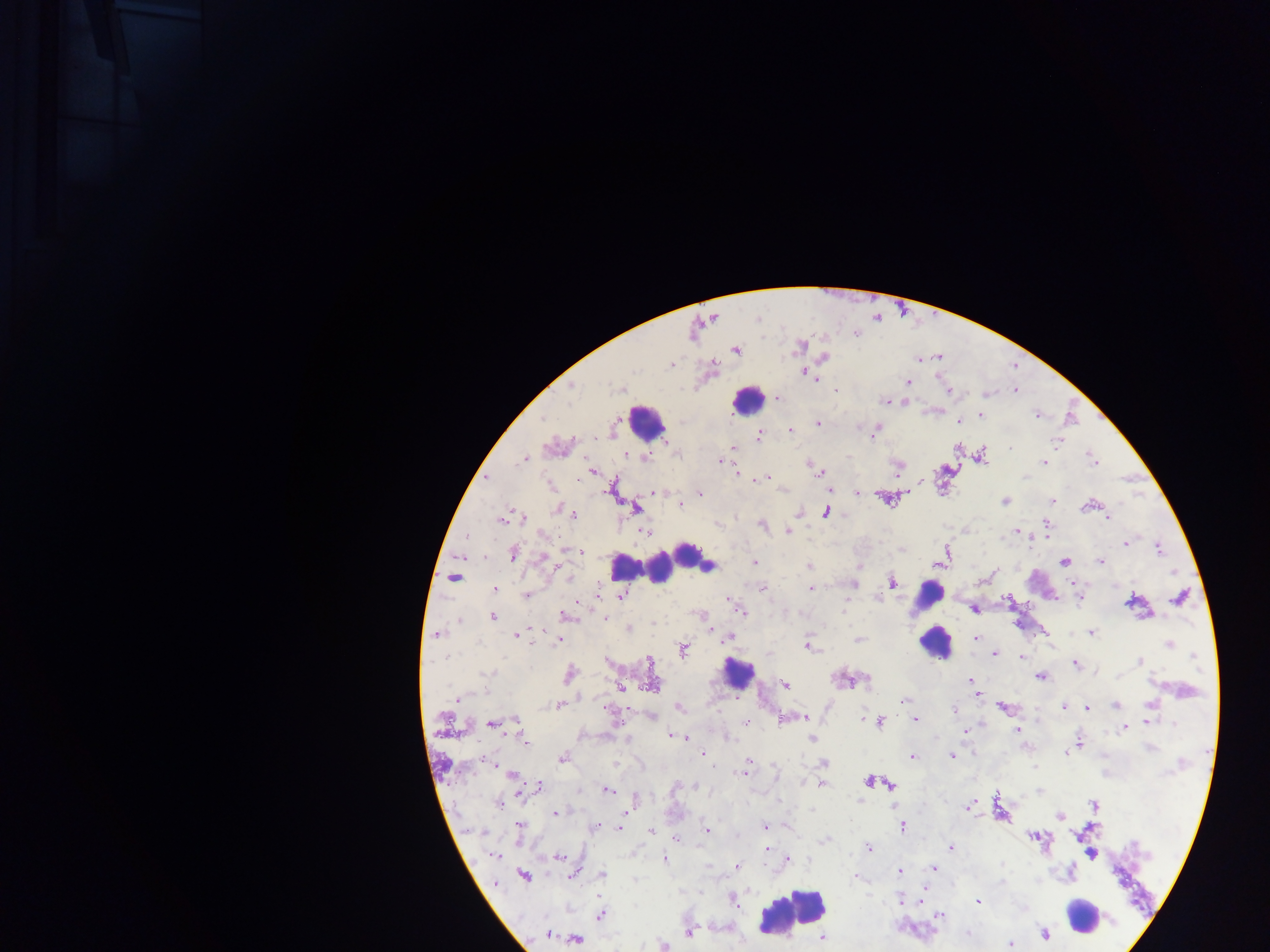

{
  "capture": "mobile-phone photograph through a microscope",
  "plasmodium_parasite_locations": "approximate centers as {x, y} in pixels: {736, 351}, {824, 358}, {671, 364}, {805, 373}, {907, 382}, {570, 387}, {620, 389}, {835, 390}, {1015, 390}, {949, 392}, {778, 398}, {885, 401}, {980, 414}, {1036, 415}, {541, 419}, {958, 421}, {818, 423}, {790, 430}, {874, 431}, {760, 436}, {1058, 442}, {734, 448}, {626, 453}, {981, 456}, {647, 458}, {1093, 458}, {523, 460}, {722, 461}, {1044, 462}, {898, 466}, {592, 471}, {820, 472}, {736, 473}, {1025, 476}, {766, 477}, {486, 478}, {550, 485}, {611, 488}, {657, 492}, {857, 493}, {701, 494}, {885, 498}, {1052, 500}, {1005, 501}, {680, 505}, {1086, 506}, {558, 509}, {635, 509}, {798, 512}, {826, 513}, {573, 515}, {1107, 517}, {523, 518}, {501, 520}, {762, 525}, {1046, 525}, {788, 531}, {1017, 531}, {644, 532}, {544, 535}, {1125, 543}, {1158, 548}, {570, 550}, {579, 551}, {513, 553}, {544, 557}, {1101, 561}, {755, 562}, {1064, 562}, {809, 566}, {454, 577}, {569, 578}, {891, 582}, {853, 585}, {763, 588}, {495, 589}, {811, 589}, {527, 594}, {621, 596}, {1079, 598}, {1179, 598}, {1132, 602}, {844, 609}, {973, 609}, {740, 611}, {567, 615}, {699, 615}, {493, 617}, {605, 619}, {460, 620}, {629, 629}, {1092, 633}, {437, 634}, {516, 635}, {728, 637}, {976, 638}, {858, 639}, {558, 640}, {1170, 644}, {808, 645}, {683, 649}, {995, 653}, {1021, 657}, {649, 661}, {1140, 661}, {1076, 665}, {486, 674}, {570, 674}, {1041, 676}, {867, 681}, {971, 681}, {784, 685}, {620, 687}, {979, 695}, {456, 700}, {904, 700}, {1151, 704}, {558, 705}, {1115, 705}, {1002, 707}, {1064, 707}, {1087, 707}, {680, 708}, {954, 709}, {652, 717}, {804, 717}, {863, 718}, {785, 719}, {515, 720}, {916, 720}, {1149, 721}, {746, 722}, {879, 722}, {492, 723}, {1173, 724}, {1125, 728}, {965, 731}, {1017, 731}, {674, 736}, {682, 737}, {728, 738}, {812, 738}, {526, 742}, {1078, 742}, {1150, 748}, {1066, 753}, {703, 754}, {952, 756}, {912, 757}, {562, 758}, {821, 759}, {486, 760}, {748, 762}, {615, 763}, {824, 764}, {1035, 767}, {743, 773}, {512, 775}, {869, 781}, {822, 785}, {889, 785}, {539, 786}, {675, 787}, {695, 787}, {607, 790}, {998, 796}, {634, 801}, {859, 801}, {499, 802}, {1094, 804}, {968, 807}, {811, 810}, {556, 813}, {1060, 816}, {764, 826}, {520, 827}, {621, 827}, {903, 827}, {595, 828}, {707, 830}, {652, 832}, {1034, 837}, {675, 838}, {824, 840}, {951, 848}, {766, 849}, {869, 849}, {1092, 855}, {494, 856}, {559, 857}, {664, 859}, {789, 859}, {708, 866}, {737, 867}, {934, 868}, {899, 872}, {574, 874}, {603, 874}, {524, 875}, {856, 878}, {1002, 882}, {900, 900}, {733, 901}, {978, 902}, {601, 914}, {939, 914}, {689, 933}, {1045, 934}, {547, 935}, {822, 938}, {576, 939}, {1010, 944}, {664, 946}",
  "leukocyte_locations": "approximate centers as {x, y} in pixels: {747, 400}, {646, 422}, {688, 552}, {621, 566}, {659, 568}, {708, 570}, {927, 595}, {929, 622}, {934, 643}, {737, 673}, {793, 914}, {1082, 915}",
  "preparation": "thick blood smear",
  "image_size": "1270×952 pixels",
  "field_of_view": "single",
  "country": "Ghana"
}